Locate every blood parasite and identify its species.
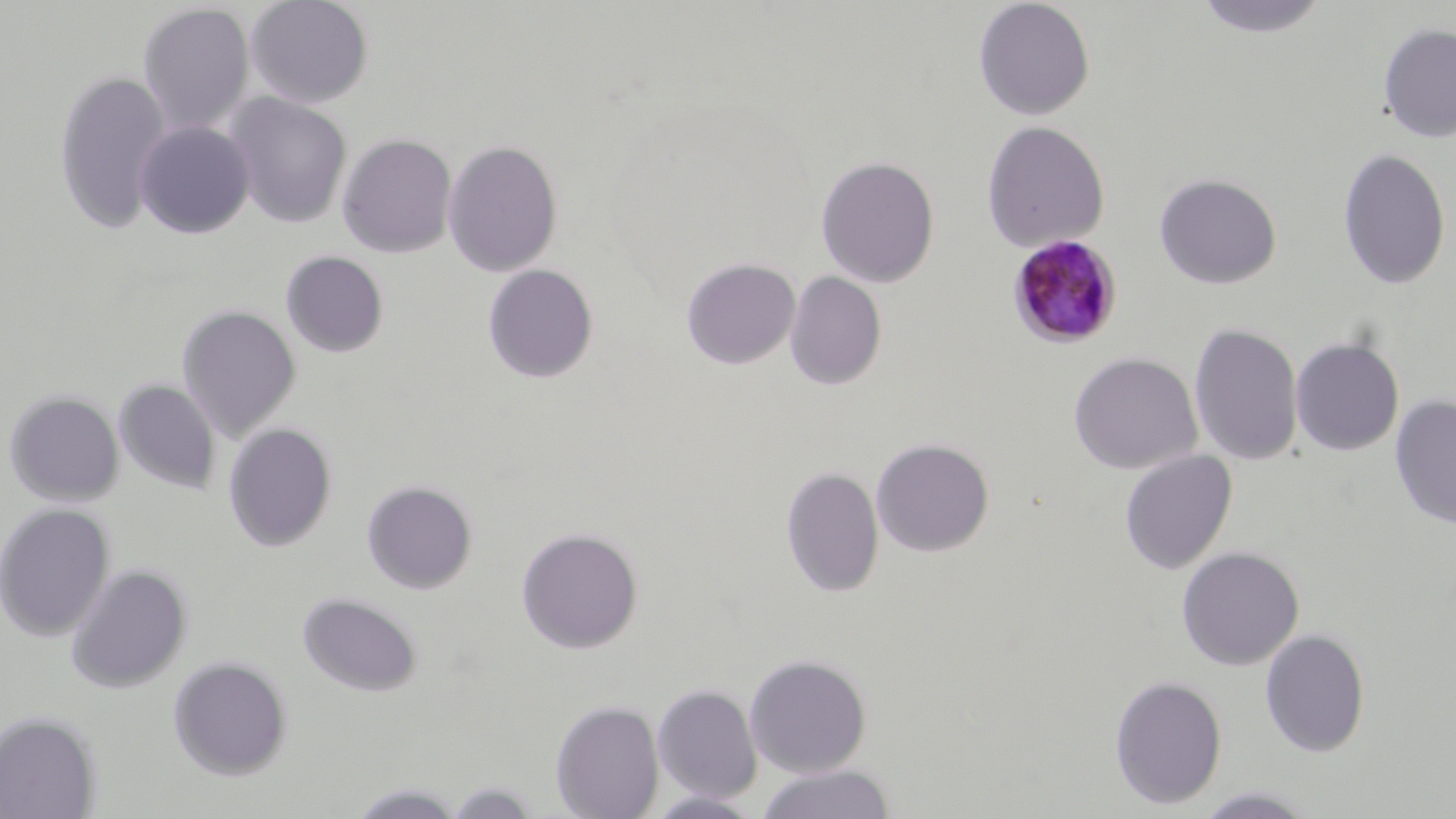

Approximate bounding boxes as (x1, y1, x2, y2) in pixels.
Plasmodium malariae-infected red blood cells: (1008, 234, 1124, 349).
No Plasmodium falciparum, Plasmodium ovale, Plasmodium vivax, Babesia divergens, or Trypanosoma brucei observed.

slide-level diagnosis = Plasmodium malariae
uninfected red blood cell locations = approximate bounding boxes as (x1, y1, x2, y2) in pixels: (245, 0, 374, 109), (973, 0, 1095, 120), (1193, 0, 1332, 39), (137, 3, 255, 135), (1378, 21, 1455, 143), (52, 70, 173, 234), (225, 93, 352, 228), (134, 120, 255, 238), (981, 121, 1110, 253), (337, 133, 457, 258), (443, 139, 563, 277), (1337, 147, 1452, 290), (815, 156, 940, 289), (1154, 172, 1282, 289), (280, 250, 389, 358), (681, 258, 801, 369), (482, 263, 599, 383), (785, 270, 887, 390), (177, 304, 301, 442), (1188, 322, 1304, 466), (1290, 336, 1405, 456), (1068, 352, 1202, 475), (114, 379, 221, 495), (3, 390, 124, 506), (1390, 394, 1456, 530), (222, 423, 337, 552), (870, 437, 994, 557), (1119, 449, 1238, 574), (780, 466, 885, 598), (361, 480, 478, 594), (0, 502, 115, 641), (515, 526, 644, 654), (1176, 546, 1304, 671), (66, 563, 192, 694), (297, 592, 423, 696), (1260, 629, 1371, 758), (744, 653, 872, 778), (168, 656, 293, 780), (1109, 675, 1228, 810), (653, 683, 762, 804), (550, 699, 665, 819), (0, 711, 101, 819), (756, 764, 896, 819), (440, 781, 546, 818), (345, 782, 471, 818), (1193, 786, 1320, 818), (645, 790, 765, 818)
field of view = one of a larger specimen
stain = May-Grünwald-Giemsa
modality = light microscopy
preparation = thin blood smear
image size = 1456×819 pixels
magnification = 1000x